Name the parasite shown.
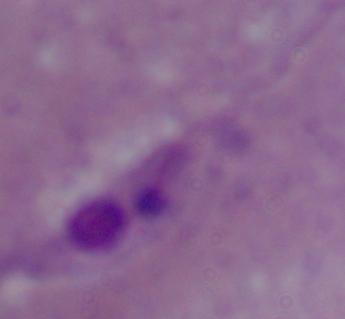

This is Leishmania.

magnification = 1000x
modality = photomicrograph